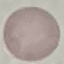
{
  "result": "no malaria parasites detected",
  "preparation": "thin blood film",
  "capture": "smartphone through the microscope eyepiece",
  "image_type": "cell patch, automatically extracted from a larger field of view and resized to 64 × 64 pixels",
  "stain": "Giemsa"
}